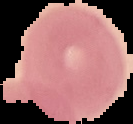 From a thin blood film. Cell region segmented out of the field of view; the surrounding area is masked to black. Image is 133×124 pixels. Malaria status: uninfected.